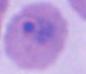
Summary:
  - Identification: Plasmodium
  - Modality: photomicrograph
  - Magnification: 400x or 1000x